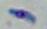

Captured at 1000x magnification. Micrograph. Toxoplasma gondii is seen.